Locate every Plasmodium parasite by life-cycle stage, and every leukocyte.
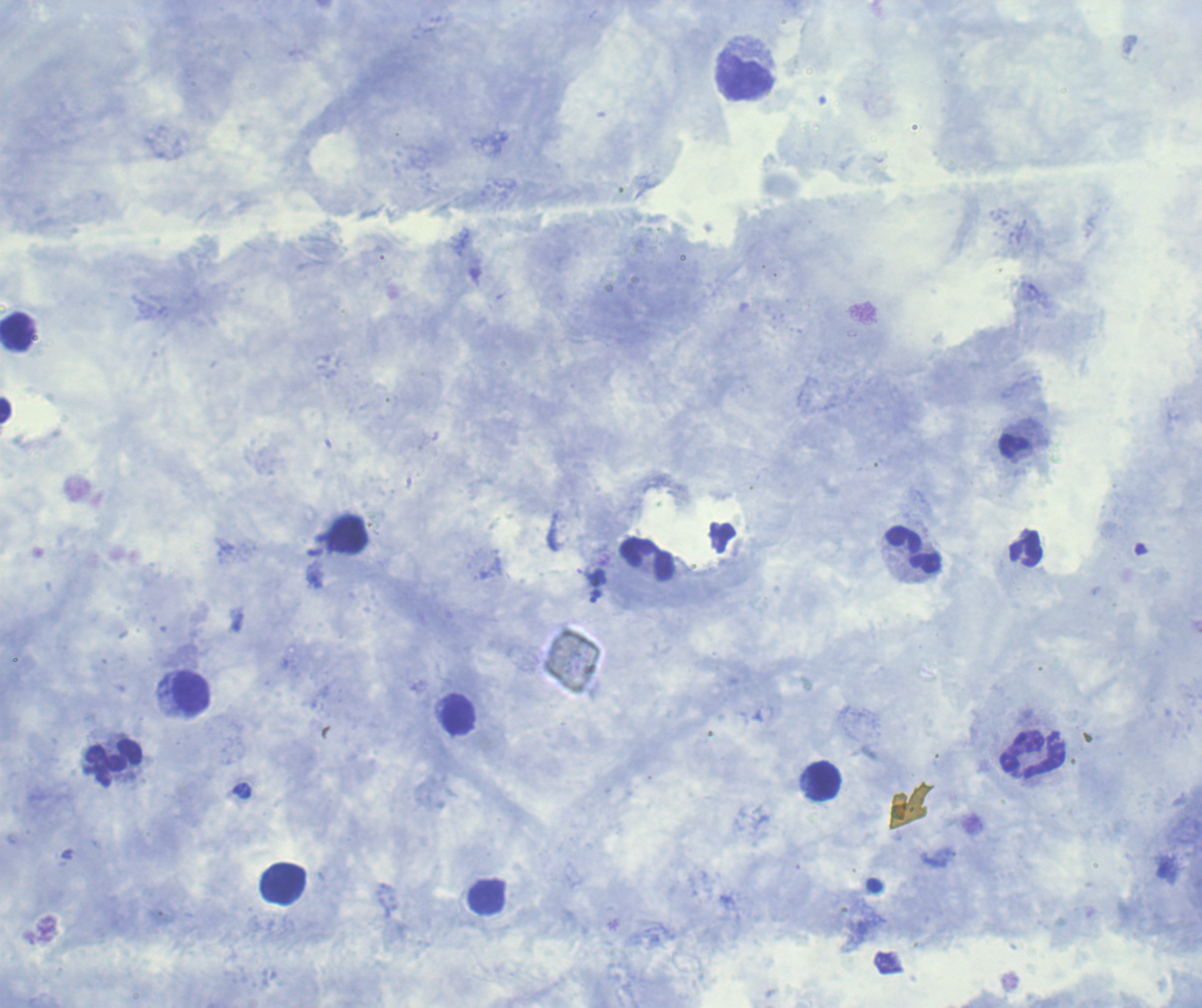
Approximate centers as {x, y} in pixels.
Trophozoites: {596, 597}.
No schizont or gametocyte forms observed.
Leukocytes: {744, 77}, {16, 331}, {5, 410}, {912, 550}, {191, 692}, {459, 713}, {1033, 754}, {114, 763}, {824, 780}, {283, 883}.

field_of_view: one from this slide
image_size: 1202×1008 pixels
magnification: 100x
context: previously used in a real diagnosis
preparation: thick blood smear
stain: Romanowsky
coloration_quality: good
background_quality: satisfactory